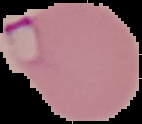 Result: malaria parasites detected. From a thin blood film. Cell region segmented out of the field of view; the surrounding area is masked to black. Image is 142×124 pixels.